Assess this cell for malaria.
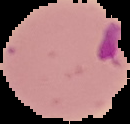

Parasitized.

{
  "image_type": "segmented cell region with the area outside set to black",
  "image_size": "130×124 pixels",
  "preparation": "thin blood film"
}